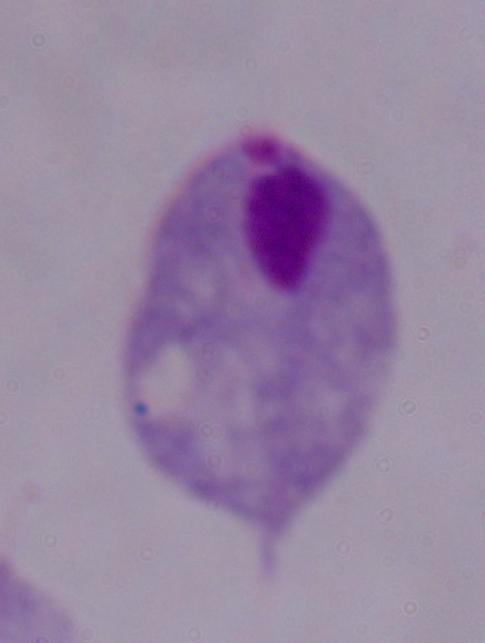
Summary:
  - Identification: trichomonad
  - Modality: micrograph
  - Magnification: 1000x